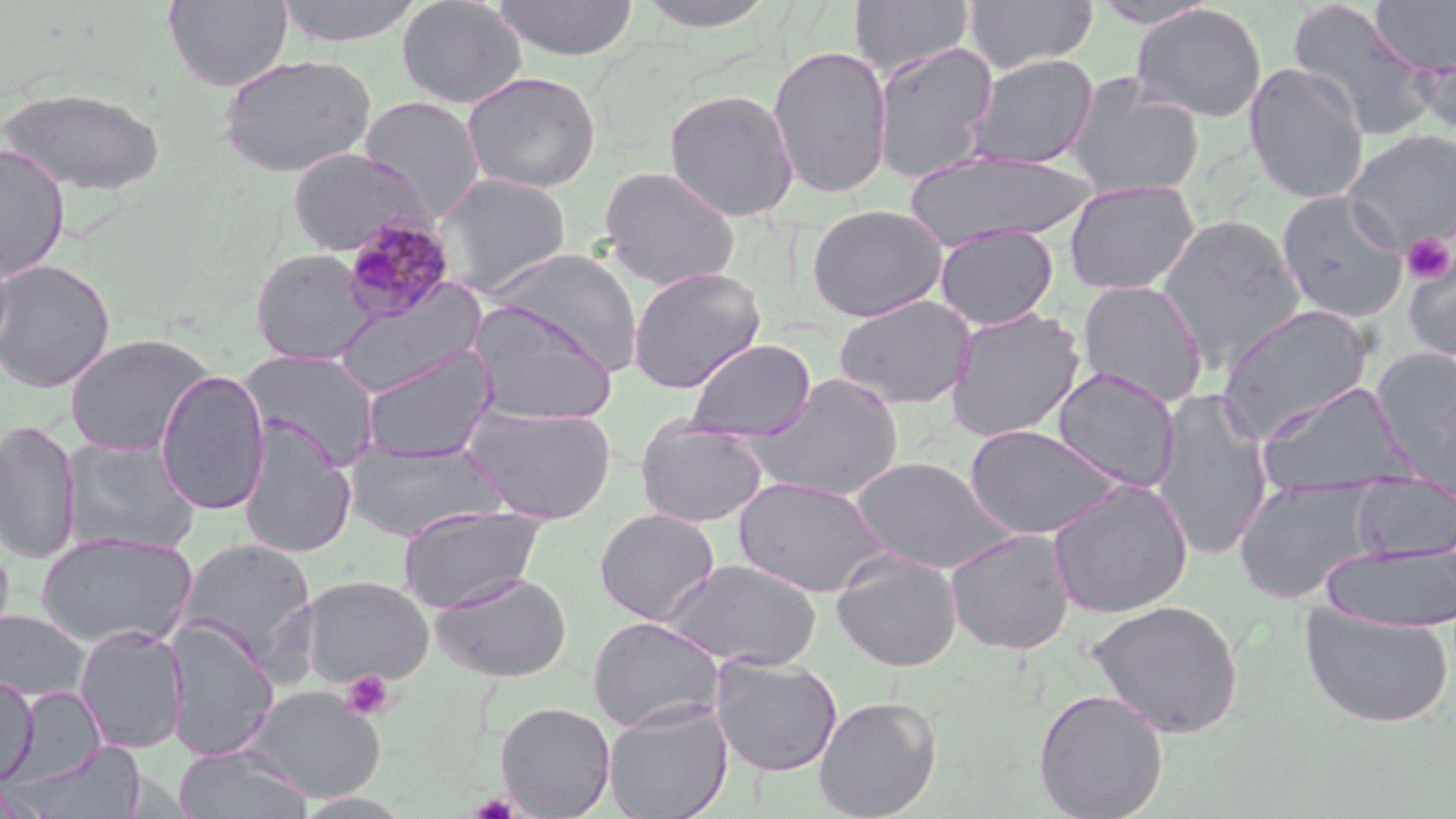

Summary:
  - Coordinate format: approximate bounding boxes as [x1, y1, x2, y2] in pixels
  - Plasmodium malariae-infected red blood cell locations: [339, 211, 457, 325]
  - Platelet locations: [1402, 233, 1455, 284], [340, 670, 395, 719], [470, 792, 519, 818]
  - Uninfected red blood cell locations: [163, 0, 293, 90], [273, 0, 427, 47], [396, 0, 527, 108], [492, 0, 640, 61], [633, 0, 782, 32], [849, 0, 975, 78], [963, 0, 1099, 74], [1287, 0, 1440, 140], [1370, 0, 1456, 77], [1088, 1, 1219, 29], [1130, 4, 1267, 122], [872, 41, 999, 183], [1413, 44, 1456, 141], [767, 45, 893, 199], [218, 53, 377, 177], [966, 53, 1099, 169], [1243, 62, 1369, 204], [462, 71, 602, 193], [1064, 76, 1205, 199], [2, 86, 166, 196], [663, 88, 800, 221], [359, 96, 485, 222], [1344, 129, 1456, 250], [0, 143, 70, 283], [286, 147, 429, 256], [903, 150, 1095, 251], [598, 166, 741, 291], [434, 173, 571, 297], [1064, 180, 1199, 295], [1276, 189, 1408, 323], [807, 203, 948, 322], [1157, 215, 1306, 369], [935, 224, 1058, 330], [487, 248, 644, 373], [250, 249, 374, 365], [1402, 250, 1456, 363], [0, 259, 116, 393], [627, 266, 766, 393], [1076, 279, 1209, 407], [333, 283, 487, 398], [833, 294, 976, 409], [468, 302, 618, 426], [1217, 304, 1373, 440], [946, 307, 1086, 443], [63, 333, 214, 457], [684, 338, 817, 441], [360, 344, 497, 464], [239, 350, 381, 471], [1383, 354, 1456, 493], [1051, 367, 1181, 492], [154, 369, 271, 515], [741, 373, 904, 502], [1255, 381, 1416, 499], [1153, 389, 1275, 560], [463, 404, 617, 524], [635, 417, 768, 528], [1, 419, 81, 564], [238, 421, 358, 559], [963, 423, 1125, 539], [62, 437, 200, 555], [343, 439, 507, 541], [850, 456, 1016, 574], [1352, 475, 1455, 563], [733, 476, 892, 597], [1234, 476, 1382, 603], [1047, 478, 1193, 619], [397, 505, 548, 614], [594, 508, 720, 625], [944, 529, 1076, 655], [35, 531, 198, 648], [175, 538, 319, 672], [0, 539, 15, 651], [1322, 543, 1456, 633], [832, 551, 962, 671], [659, 558, 822, 670], [681, 561, 835, 767], [429, 571, 572, 682], [299, 575, 433, 687], [1087, 599, 1244, 738], [1299, 602, 1454, 728], [0, 610, 90, 700], [587, 616, 726, 732], [164, 619, 279, 761], [74, 624, 189, 753], [711, 655, 843, 777], [0, 671, 39, 786], [11, 685, 108, 785], [241, 686, 387, 802], [1033, 687, 1169, 819], [813, 695, 942, 819], [603, 699, 733, 819], [495, 701, 616, 817], [17, 740, 146, 819], [172, 744, 312, 818]
  - Slide-level diagnosis: Plasmodium malariae
  - Image size: 1456×819 pixels
  - Stain: May-Grünwald-Giemsa
  - Preparation: thin blood film
  - Field of view: one of a larger specimen
  - Modality: optical microscopy
  - Magnification: 1000x